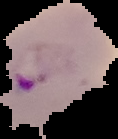

preparation: thin blood film
malaria_status: parasitized
image_type: cell region segmented out of the field of view; surrounding area masked to black
image_size: 118×139 pixels